Point out each Plasmodium parasite and each leukocyte.
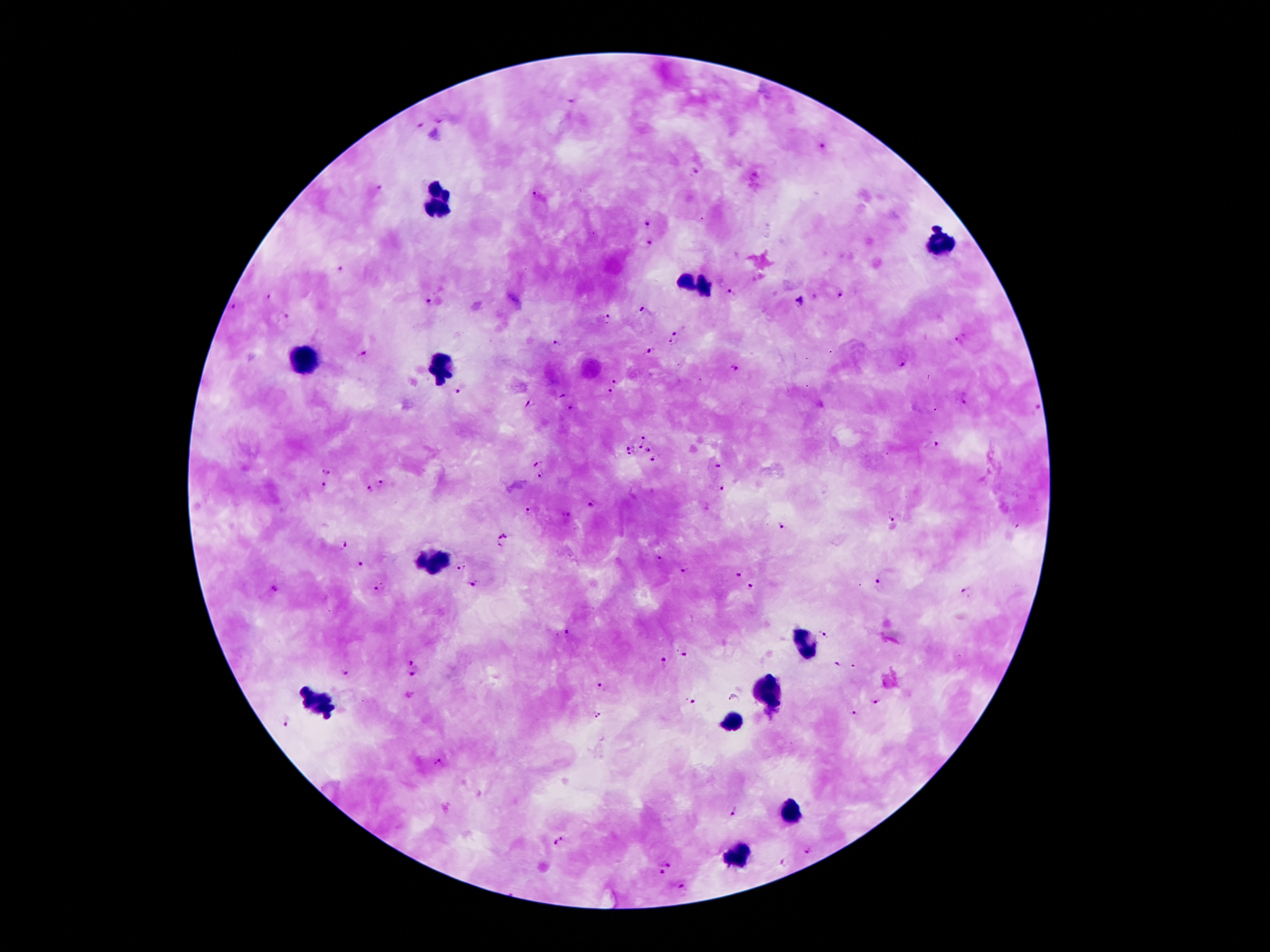

Approximate centers as [x, y] in pixels.
Plasmodium parasites: [570, 100], [440, 121], [420, 123], [823, 147], [695, 172], [379, 187], [538, 197], [647, 223], [649, 244], [342, 270], [730, 294], [842, 295], [268, 297], [801, 301], [430, 304], [234, 306], [644, 310], [287, 317], [607, 321], [676, 331], [961, 340], [557, 343], [672, 343], [651, 349], [362, 356], [901, 364], [734, 368], [615, 379], [460, 390], [610, 392], [560, 396], [964, 401], [528, 403], [570, 408], [1036, 408], [644, 435], [934, 444], [628, 447], [640, 447], [649, 448], [629, 452], [652, 461], [537, 463], [717, 465], [330, 471], [541, 475], [384, 479], [322, 487], [369, 488], [722, 489], [589, 504], [529, 511], [890, 514], [782, 525], [504, 541], [342, 544], [660, 558], [361, 563], [462, 568], [683, 571], [739, 575], [877, 580], [473, 583], [750, 585], [376, 588], [273, 589], [968, 592], [824, 633], [567, 634], [683, 650], [411, 659], [835, 664], [664, 665], [344, 671], [413, 676], [600, 686], [735, 699], [874, 700], [691, 701], [595, 713], [856, 713], [287, 720], [437, 763], [733, 810], [558, 842], [809, 850], [666, 863], [783, 863], [661, 873], [681, 887].
Leukocytes: [437, 200], [942, 242], [695, 282], [309, 360], [441, 362], [426, 561], [804, 643], [768, 690], [317, 700], [733, 721], [787, 809], [739, 855].

Patient malaria status: infected with Plasmodium falciparum. One field from this slide. Image is 1270×952 pixels. Thick blood smear. 100x magnification. Giemsa stain. Photographed through the microscope eyepiece with a smartphone camera.